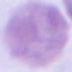

Summary:
  - Magnification: 1000x
  - Modality: micrograph
  - Identification: red blood cell